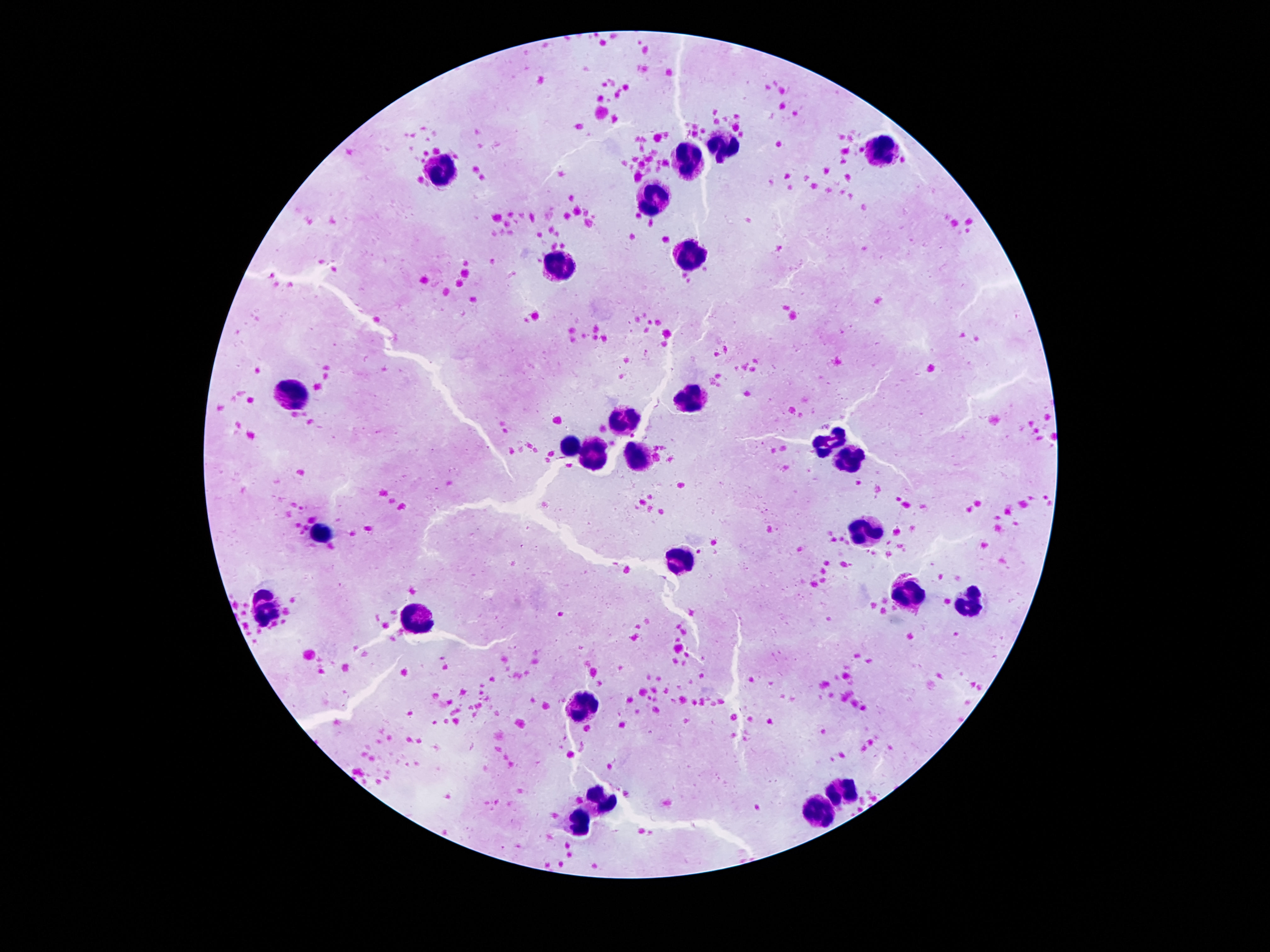
stain = Giemsa
patient malaria status = not infected
leukocyte locations = approximate object centers, in pixels from the top-left corner: (x=717, y=147), (x=883, y=148), (x=690, y=157), (x=440, y=169), (x=656, y=195), (x=685, y=251), (x=561, y=267), (x=290, y=394), (x=690, y=396), (x=627, y=422), (x=829, y=440), (x=568, y=444), (x=594, y=456), (x=640, y=457), (x=853, y=462), (x=865, y=530), (x=324, y=531), (x=683, y=557), (x=908, y=590), (x=969, y=602), (x=266, y=613), (x=413, y=622), (x=583, y=703), (x=844, y=788), (x=599, y=796), (x=822, y=809), (x=577, y=825)
magnification = 100x
field of view = single
preparation = thick blood smear
image size = 1270×952 pixels
capture = smartphone camera through the microscope eyepiece